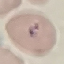

{
  "result": "malaria parasites identified",
  "preparation": "thin blood smear",
  "image_type": "automatically extracted cell patch, resized to 64 × 64 pixels",
  "capture": "smartphone camera at the microscope eyepiece",
  "stain": "Giemsa"
}